Assess this cell for malaria.
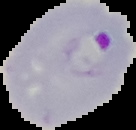
Parasitized.

preparation = thin blood film
image type = cell region segmented out of the field of view; surrounding area masked to black
image size = 136×130 pixels